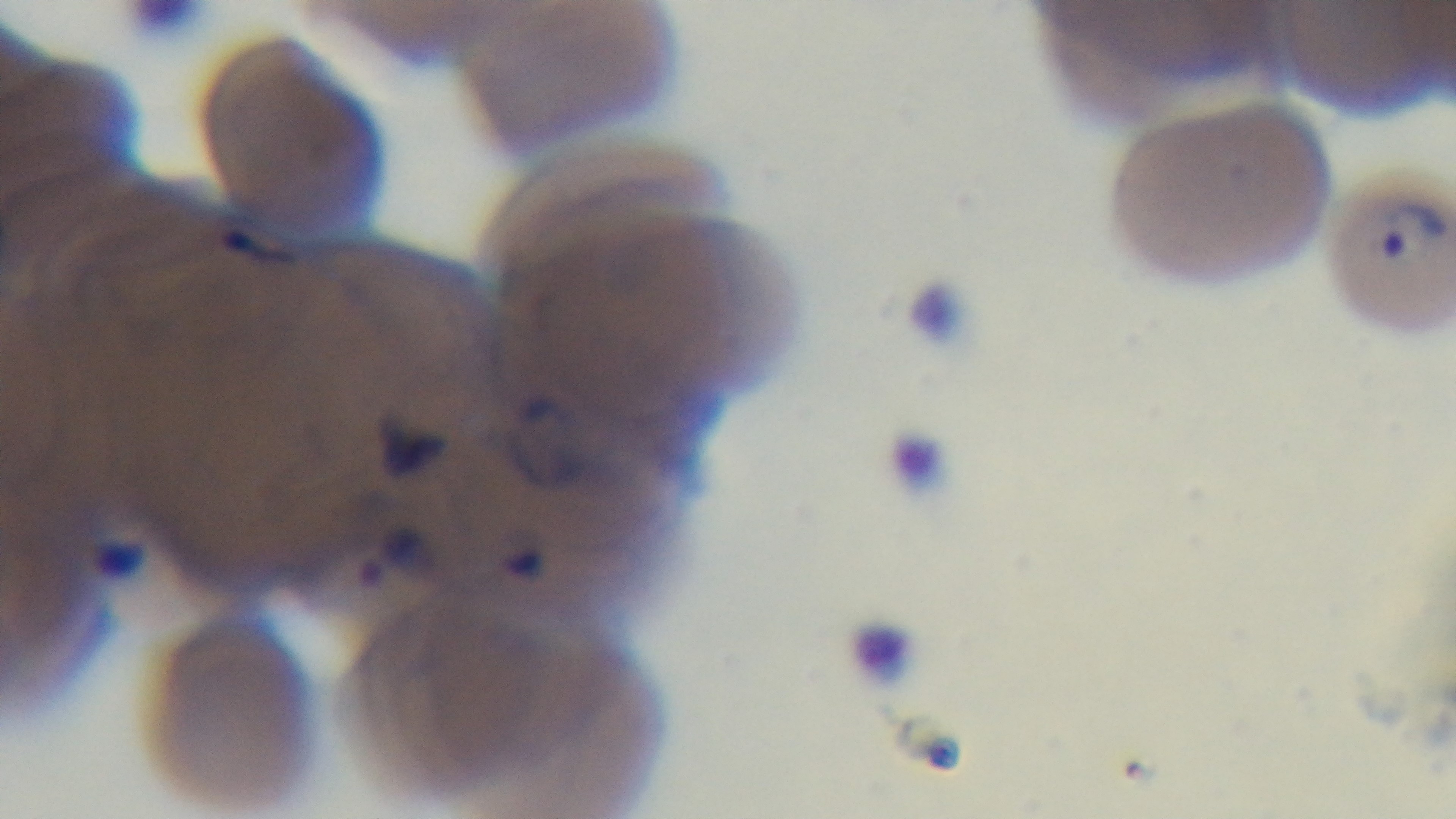

Light microscopy. Giemsa-stained. Captured with a mounted 4K digital camera. Malaria status: infected. Single field of view. 100x oil-immersion objective. Preparation: thin.